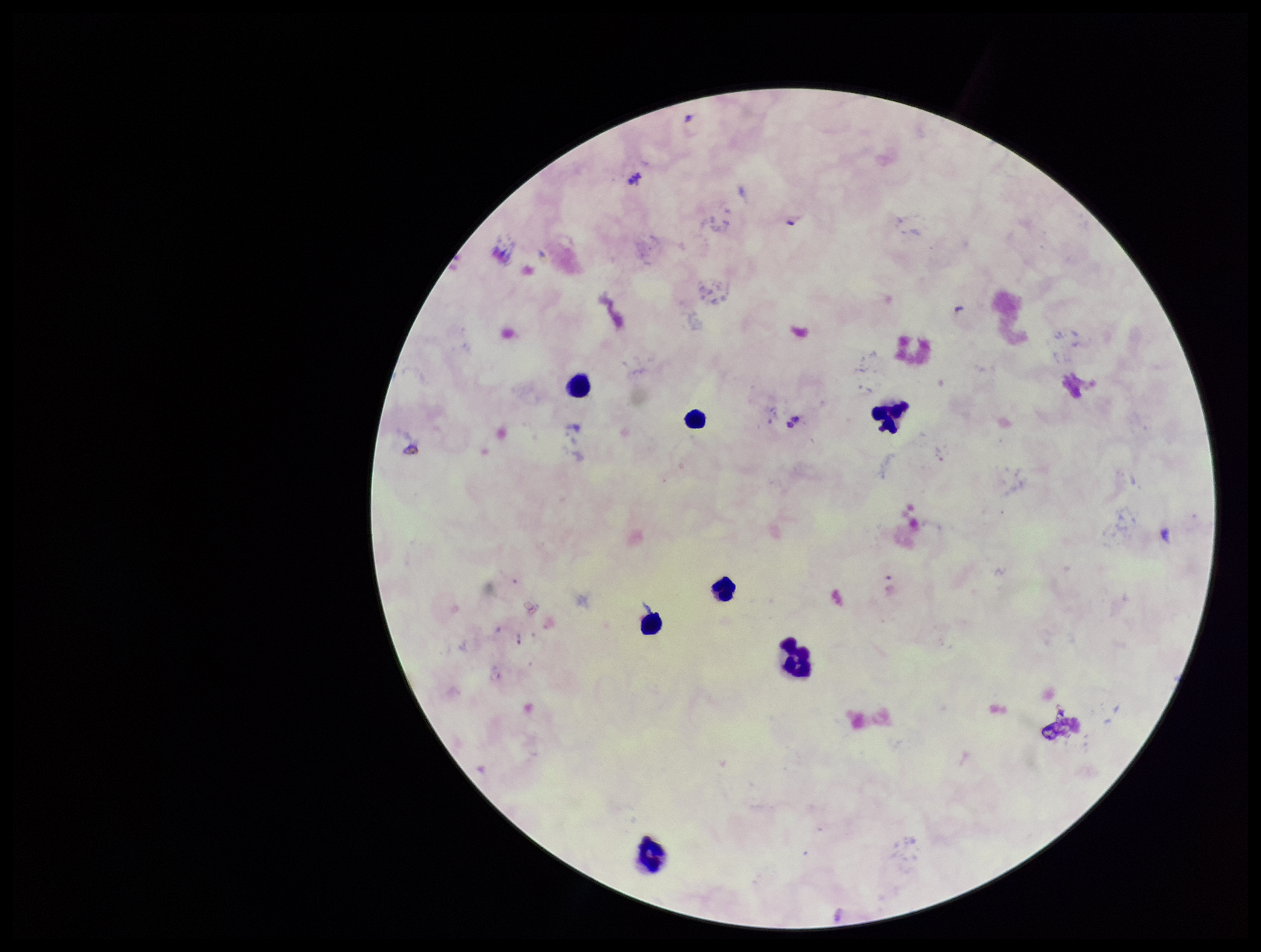

Summary:
  - Leukocyte count: 7
  - Plasmodium parasites: none seen
  - Parasite count: 0
  - Patient malaria status: infected
  - Capture: smartphone photograph through the microscope eyepiece
  - Preparation: thick blood smear
  - Image size: 1261×952 pixels
  - Stain: Giemsa
  - Field of view: one from this slide
  - Species reported for this patient: Plasmodium falciparum